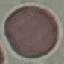

Result: negative for malaria parasites. Automatically extracted cell patch, resized to 64 × 64 pixels. Photographed with a smartphone camera at the microscope eyepiece. Thin smear of blood. Giemsa-stained preparation.